Assess this cell for malaria.
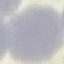

Uninfected.

Photographed with a smartphone camera at the microscope eyepiece. Automatically extracted cell patch, resized to 64 × 64 pixels. Thin smear of blood. Giemsa-stained preparation.